Name the parasite shown.
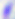

This is Toxoplasma gondii.

Micrograph. 400x magnification.